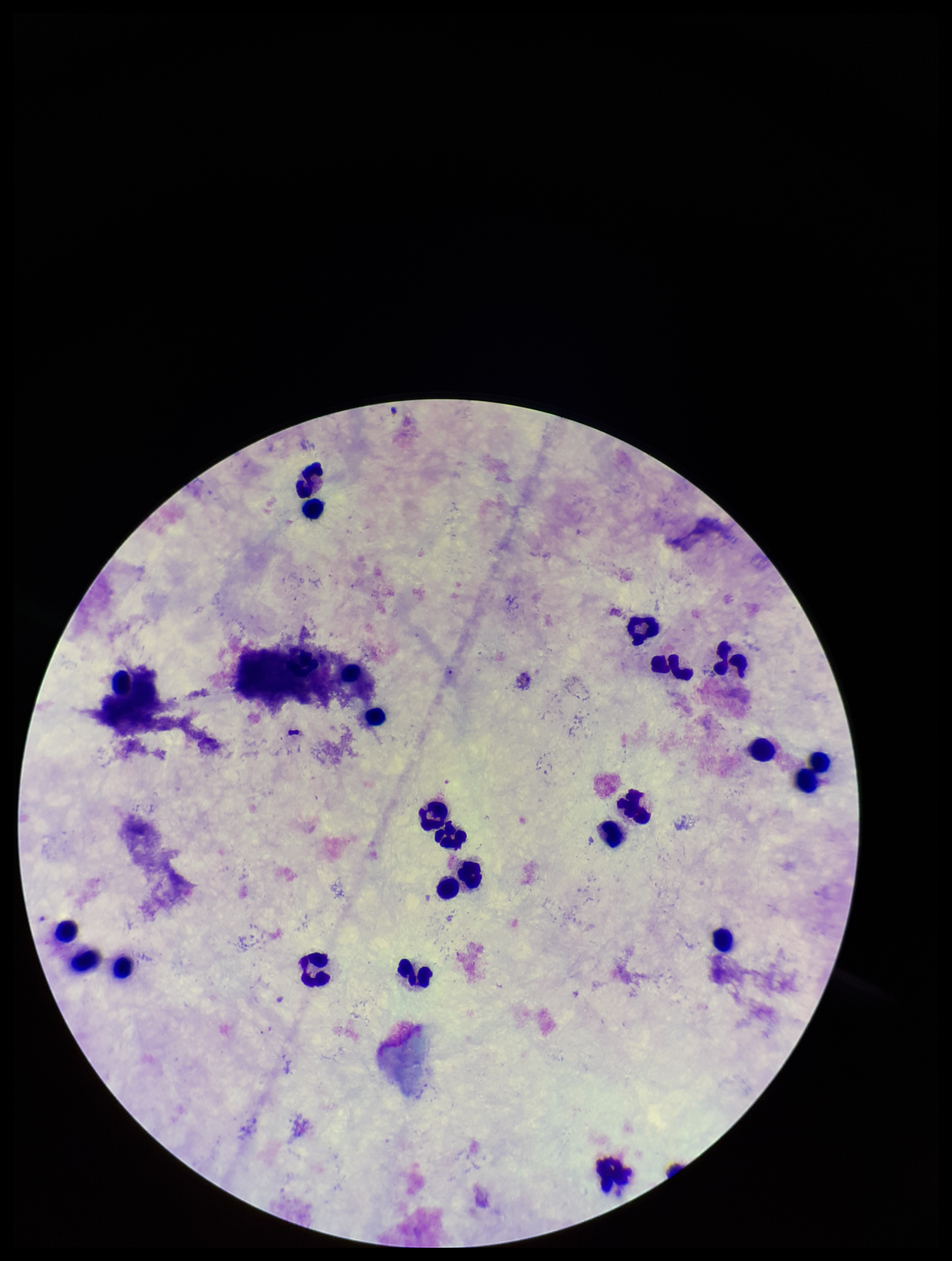 Parasite count: 0. Patient malaria status: negative. Giemsa stain. Smartphone photograph taken through the eyepiece of a microscope. Preparation: thick smear. Leukocyte count: 24. Image is 952×1261 pixels. One field from this slide. Plasmodium parasites: none detected.